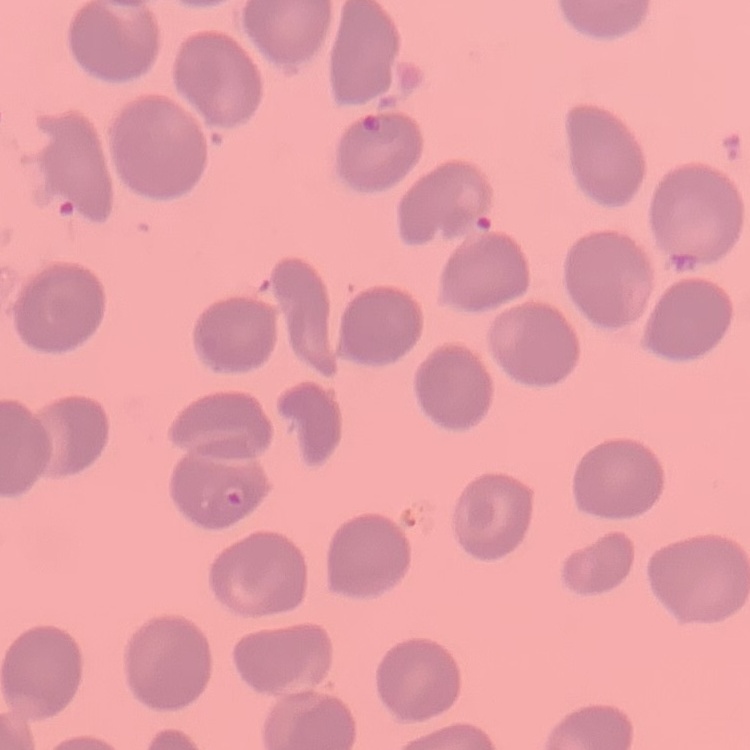

Summary:
  - Erythrocyte morphology: no rouleaux formation
  - Image type: square crop of a larger photomicrograph
  - Stain: Field's or Giemsa
  - Preparation: thin blood smear